Name the parasite shown.
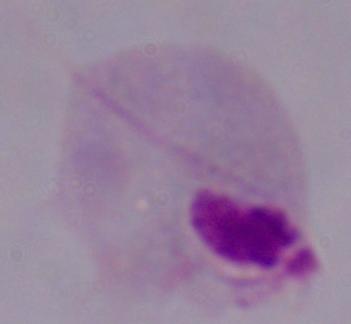

This is a trichomonad.

Summary:
  - Magnification: 1000x
  - Modality: micrograph